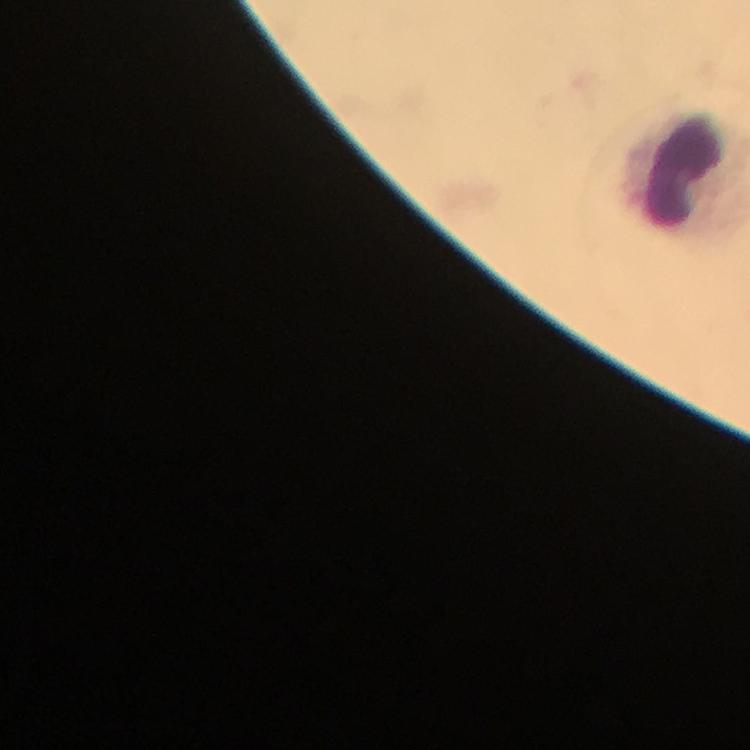
Approximate centers as (x, y) in pixels. Leukocyte locations: (676, 176). Plasmodium parasites: none detected. From a malaria diagnostic workup. Thick smear. Image is 750×750 pixels. Photographed through the microscope with a smartphone camera. Giemsa-stained preparation. Immersion oil was used. A crop from one field of view. At 100x magnification.